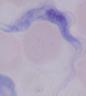

A trypanosome is shown. Photomicrograph. 1000x magnification.